Identify the parasite.
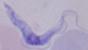
A trypanosome.

magnification: 1000x
modality: micrograph